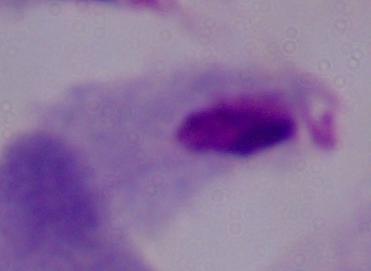

Photomicrograph. Captured at 1000x magnification. A trichomonad is shown.